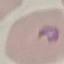

Result: malaria parasites identified. Thin blood film. Acquired by smartphone through the microscope eyepiece. Giemsa stain. Cell patch, automatically extracted from a larger field of view and resized to 64 × 64 pixels.